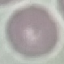

Summary:
  - Malaria status: uninfected
  - Preparation: thin blood smear
  - Stain: Giemsa
  - Capture: smartphone through the microscope eyepiece
  - Image type: cell patch, automatically extracted from a larger field of view and resized to 64 × 64 pixels